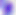
Summary:
  - Magnification: 400x
  - Identification: Toxoplasma gondii
  - Modality: photomicrograph